State the preparation type.
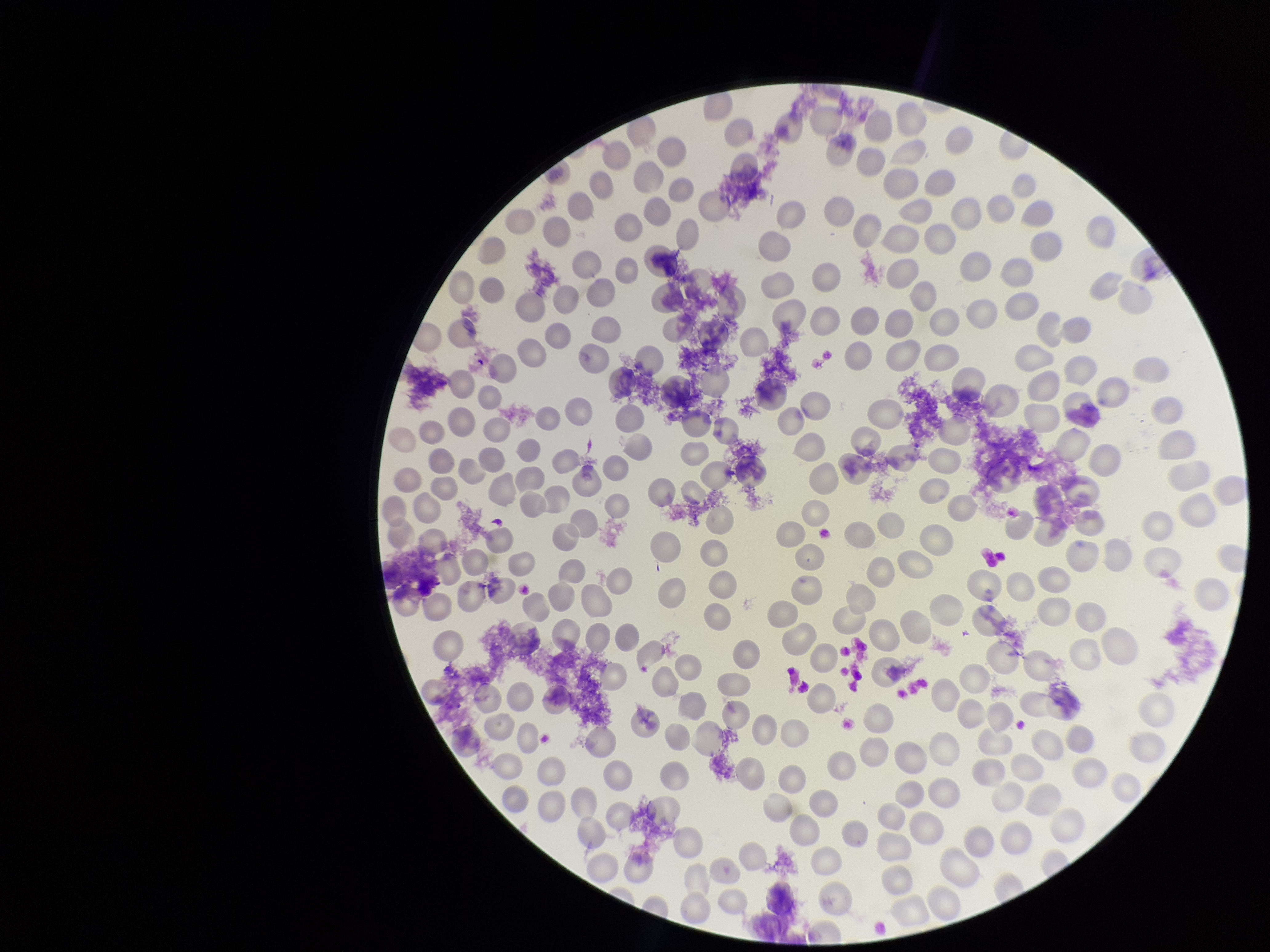

Thin.

field_of_view: one from this slide
capture: smartphone photograph through the microscope eyepiece
parasitized_red_blood_cells: none identified
red_blood_cell_count: 190
patient_malaria_status: negative
parasitized_red_blood_cell_count: 0
image_size: 1270×952 pixels
stain: Giemsa